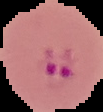 Result: malaria parasites identified. Segmented cell region on a black background. Image is 103×112 pixels. From a thin blood smear.